Report the malaria status of this cell.
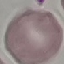
Uninfected.

Giemsa-stained preparation. Thin blood film. Photographed with a smartphone camera at the microscope eyepiece. Cell patch, automatically extracted from a larger field of view and resized to 64 × 64 pixels.